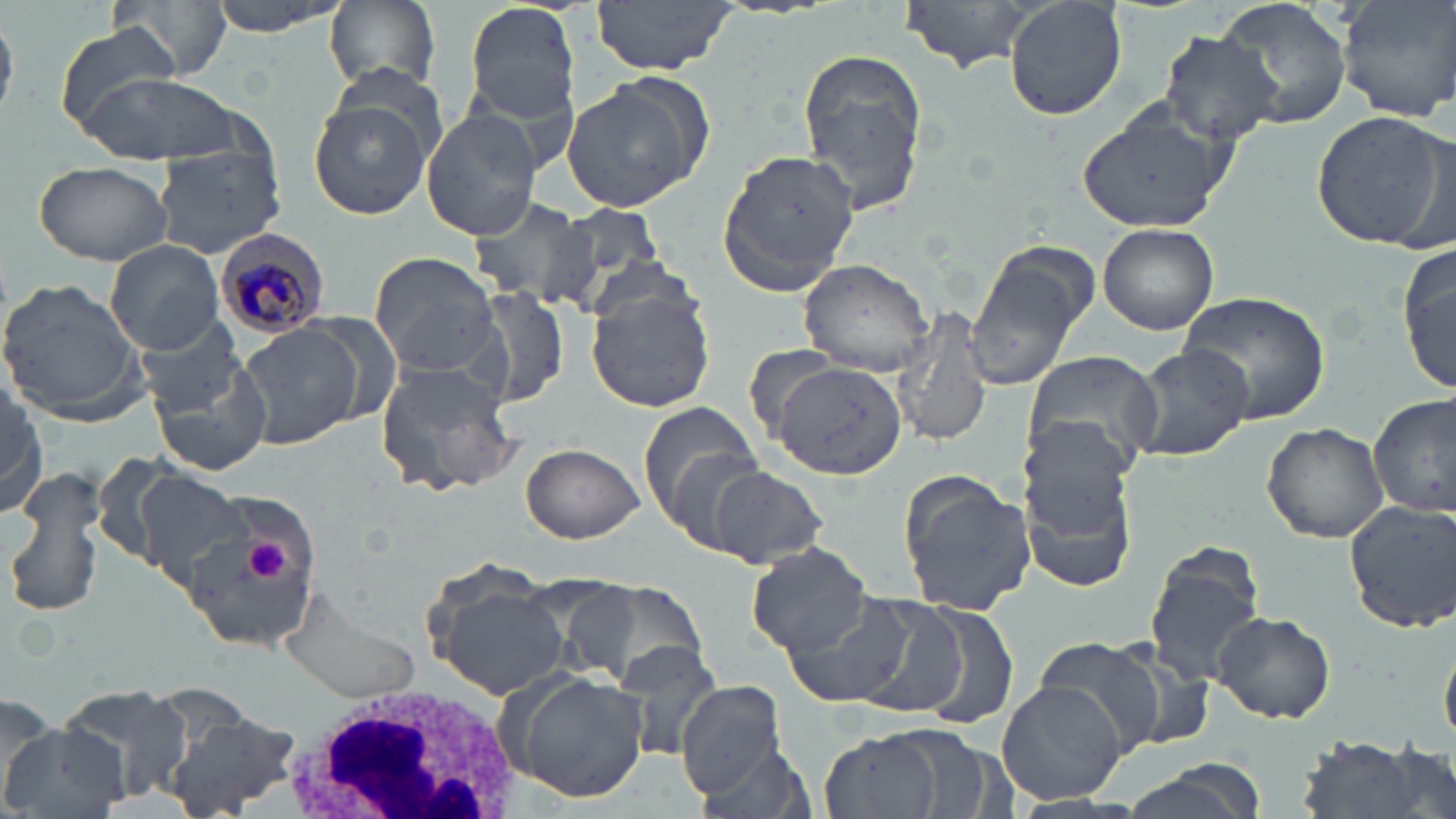
slide_level_diagnosis: Plasmodium malariae
white_blood_cell_locations: 'approximate bounding boxes as (x1,y1)-(x2,y2) corner pairs in pixels: (277,684)-(530,818)'
field_of_view: single
uninfected_red_blood_cell_locations: 'approximate bounding boxes as (x1,y1)-(x2,y2) corner pairs in pixels: (206,0)-(349,37), (326,0)-(441,94), (901,0)-(1044,73), (1003,0)-(1128,120), (1216,0)-(1355,132), (1335,0)-(1456,123), (464,1)-(584,127), (593,1)-(737,80), (116,2)-(232,81), (53,20)-(184,130), (1156,30)-(1285,145), (797,46)-(930,212), (1107,49)-(1261,205), (78,72)-(241,165), (561,80)-(702,212), (307,96)-(437,221), (1076,100)-(1240,237), (422,109)-(546,240), (1311,109)-(1448,249), (153,146)-(287,259), (715,149)-(861,294), (33,160)-(173,266), (467,194)-(595,307), (552,203)-(669,306), (1097,222)-(1219,335), (1398,235)-(1454,396), (104,240)-(224,354), (965,245)-(1094,393), (368,250)-(503,378), (799,258)-(934,375), (0,278)-(149,424), (586,283)-(716,414), (473,287)-(573,410), (1176,290)-(1331,427), (893,306)-(993,449), (136,317)-(250,414), (237,323)-(367,451), (1128,345)-(1252,463), (1021,351)-(1164,475), (148,354)-(275,479), (768,359)-(906,479), (376,361)-(522,499), (1,380)-(47,519), (1370,393)-(1454,519), (637,404)-(766,541), (1262,423)-(1387,542), (1019,442)-(1137,590), (520,443)-(644,543), (3,466)-(109,622), (706,466)-(827,567), (132,470)-(255,590), (898,472)-(1035,614), (1341,498)-(1456,633), (176,511)-(316,652), (747,542)-(876,658), (1145,544)-(1269,689), (425,571)-(571,700), (561,579)-(707,692), (282,589)-(420,705), (779,592)-(919,708), (830,593)-(971,716), (914,603)-(1021,732), (1209,608)-(1337,724), (1441,626)-(1456,752), (1029,635)-(1173,761), (616,638)-(724,763), (502,670)-(650,802), (996,679)-(1129,805), (675,681)-(788,801), (56,683)-(193,803), (0,695)-(60,808), (166,710)-(300,817), (0,724)-(129,819), (821,728)-(949,819), (1289,736)-(1442,819), (691,738)-(819,819), (1119,761)-(1265,819)'
modality: optical microscopy
stain: May-Grünwald-Giemsa
image_size: 1456×819 pixels
magnification: 1000x
plasmodium_malariae_infected_red_blood_cell_locations: 'approximate bounding boxes as (x1,y1)-(x2,y2) corner pairs in pixels: (215,229)-(330,342)'
preparation: thin blood film
platelet_locations: 'approximate bounding boxes as (x1,y1)-(x2,y2) corner pairs in pixels: (234,531)-(300,591)'